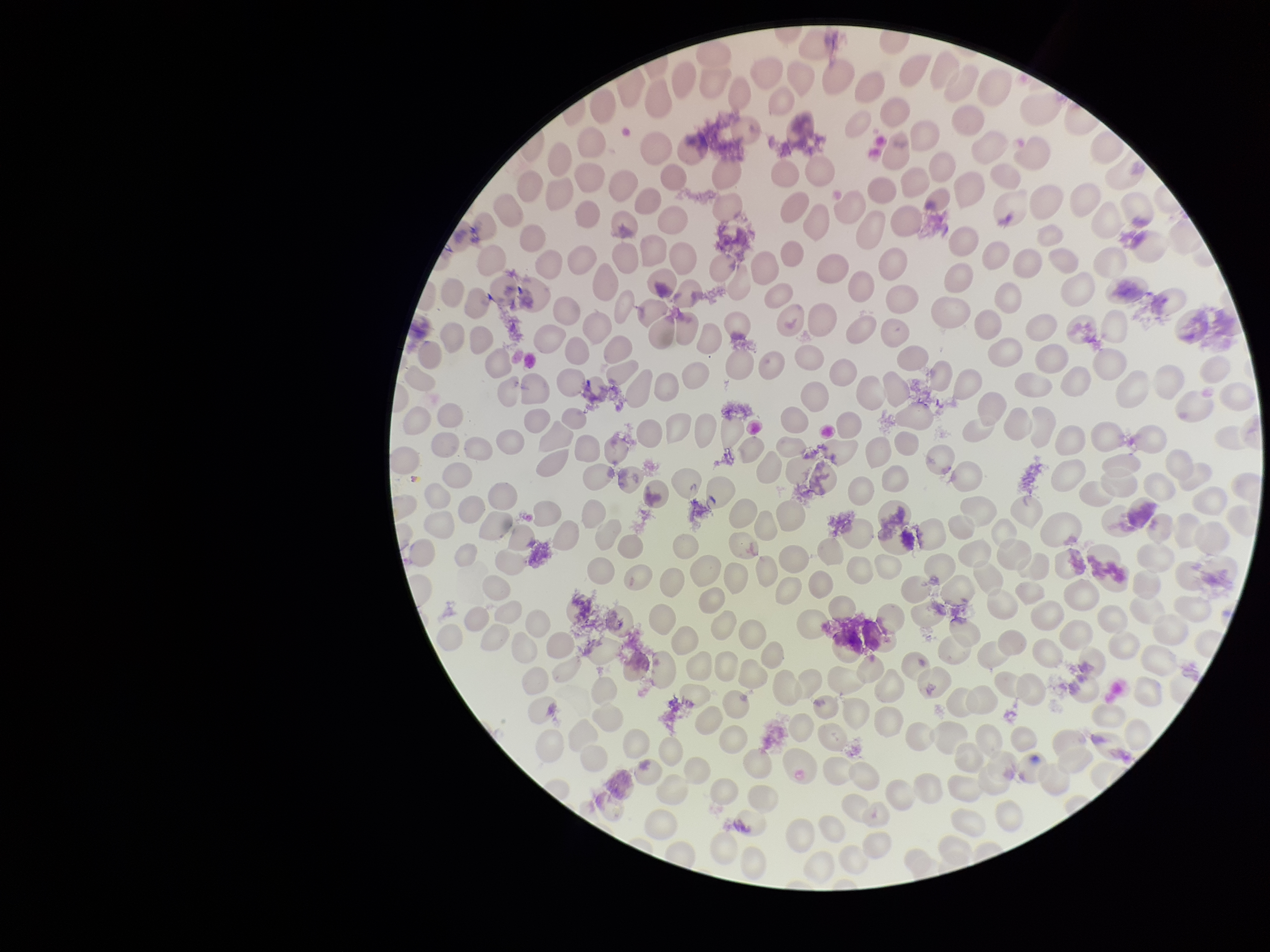

parasitized red blood cell count = 0
preparation = thin
parasitized red blood cells = none detected
patient malaria status = negative
red blood cell count = 202
stain = Giemsa
capture = smartphone photograph through the microscope eyepiece
field of view = one from this slide
image size = 1270×952 pixels